Classify this cell by malaria status.
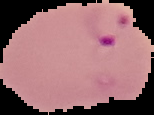
Parasitized.

preparation = thin blood film
image type = segmented cell region on a black background
image size = 154×115 pixels